State which cell type is depicted.
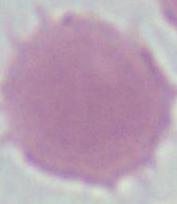

This is an erythrocyte.

Micrograph. Captured at 1000x magnification.